Report the malaria status of this cell.
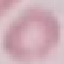
Uninfected.

{
  "stain": "Giemsa",
  "preparation": "thin blood film",
  "image_type": "automatically extracted cell patch, resized to 64 × 64 pixels",
  "capture": "smartphone through the microscope eyepiece"
}